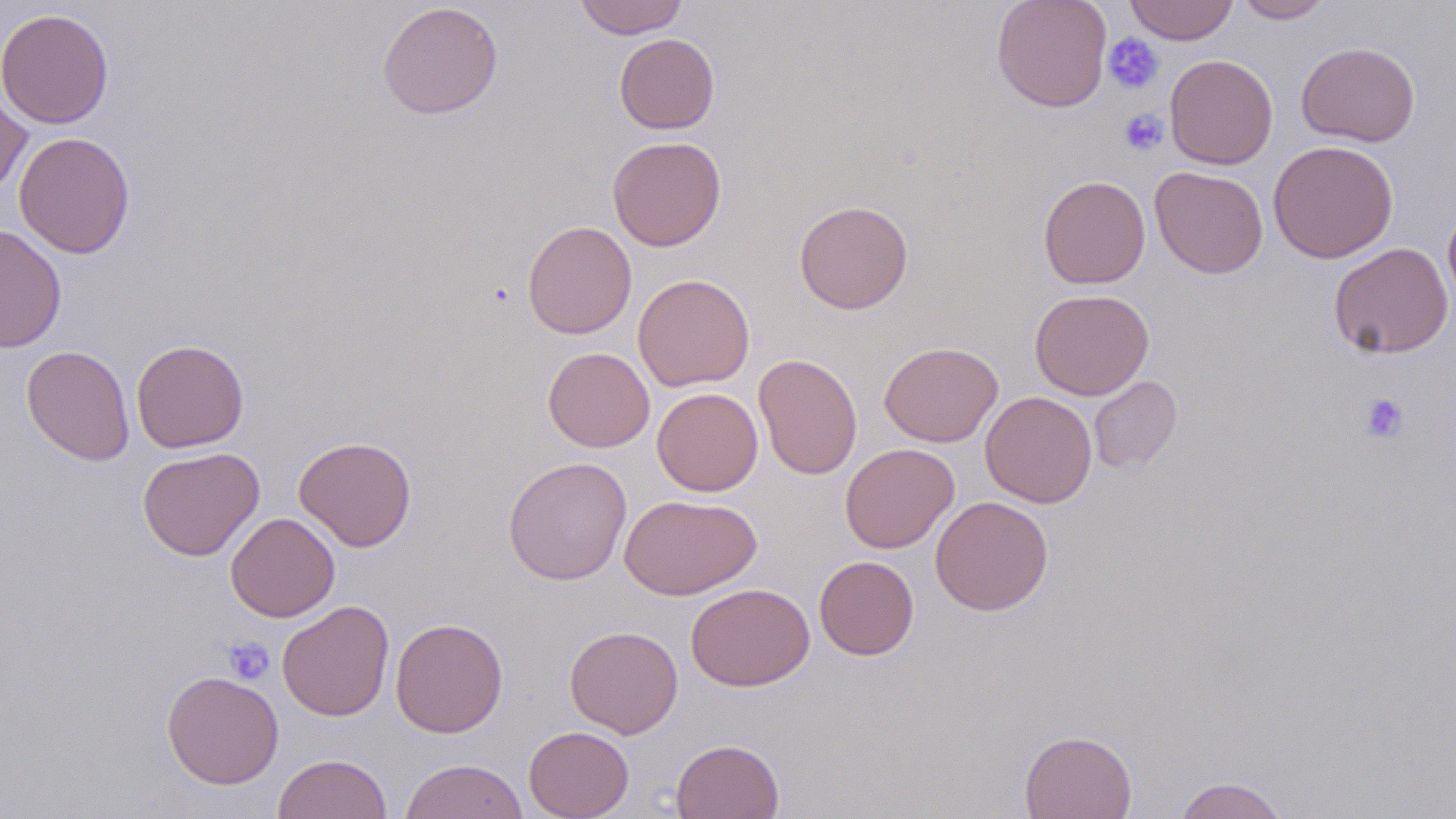
Approximate bounding boxes as [x1, y1, x2, y2] in pixels. Platelet locations: [1102, 32, 1164, 94], [1119, 109, 1167, 155], [1359, 393, 1409, 444], [222, 636, 275, 685]. Uninfected red blood cell locations: [573, 0, 688, 39], [991, 0, 1112, 112], [1125, 0, 1238, 45], [1234, 0, 1334, 23], [377, 2, 503, 119], [0, 7, 114, 130], [614, 33, 719, 134], [1296, 41, 1421, 147], [1164, 54, 1278, 170], [0, 81, 33, 199], [14, 131, 136, 258], [607, 135, 727, 251], [1268, 139, 1398, 264], [1150, 166, 1268, 279], [1038, 175, 1150, 289], [794, 199, 913, 314], [1442, 201, 1456, 315], [522, 221, 637, 339], [0, 223, 67, 353], [1328, 242, 1454, 359], [633, 273, 755, 392], [1030, 288, 1154, 400], [131, 339, 249, 453], [878, 341, 1004, 447], [22, 345, 134, 466], [543, 347, 654, 452], [753, 354, 864, 480], [1089, 376, 1182, 473], [652, 388, 763, 496], [980, 391, 1097, 508], [293, 435, 417, 551], [840, 443, 959, 553], [137, 446, 265, 561], [503, 456, 632, 584], [619, 494, 761, 600], [930, 496, 1053, 615], [225, 512, 340, 622], [814, 556, 919, 659], [685, 583, 815, 691], [277, 600, 394, 721], [390, 617, 509, 738], [564, 625, 683, 738], [161, 671, 284, 789], [523, 725, 634, 819], [1019, 729, 1137, 819], [670, 738, 784, 818], [272, 753, 394, 818], [400, 758, 528, 819], [1173, 775, 1289, 819]. Slide-level diagnosis: no evidence of blood parasites. Captured at 1000x magnification. May-Grünwald-Giemsa stain. Thin blood smear. Image is 1456×819 pixels. One field of a larger specimen. Light microscopy.